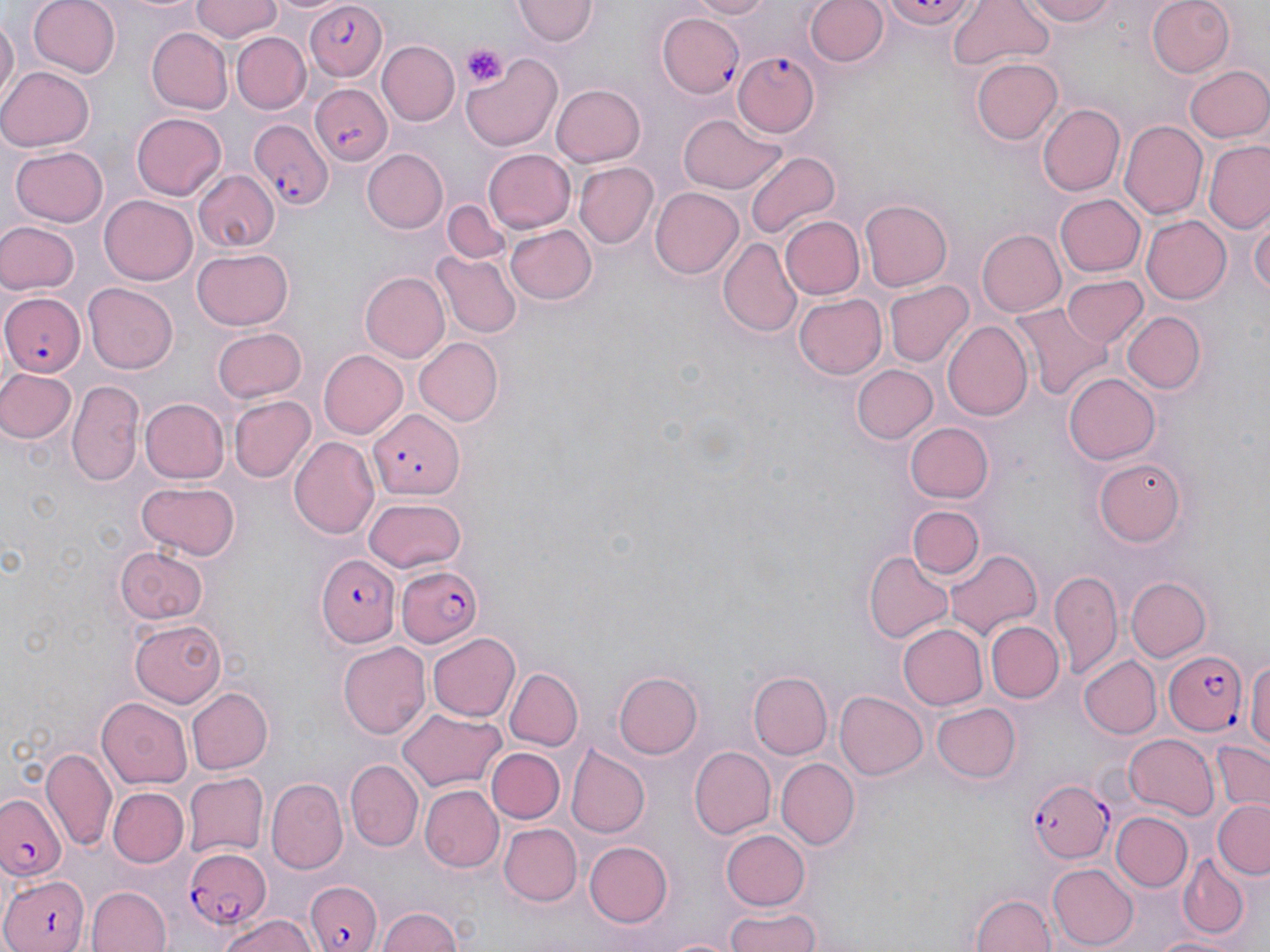

Summary:
  - Coordinate format: approximate bounding boxes as (x1, y1, x2, y2) in pixels
  - Plasmodium falciparum-infected red blood cell locations: (881, 0, 978, 30), (303, 3, 386, 82), (732, 50, 819, 137), (310, 85, 392, 166), (247, 117, 332, 213), (0, 289, 84, 378), (371, 409, 464, 495), (315, 555, 400, 646), (395, 565, 483, 645), (1164, 649, 1251, 736), (1028, 778, 1113, 864), (0, 794, 65, 884), (180, 842, 271, 936), (0, 874, 90, 952), (304, 878, 383, 952)
  - Platelet locations: (461, 43, 508, 91)
  - Uninfected red blood cell locations: (26, 0, 119, 78), (190, 0, 282, 44), (691, 0, 775, 20), (805, 0, 890, 70), (1018, 0, 1124, 26), (1147, 0, 1234, 76), (515, 1, 600, 45), (948, 1, 1054, 71), (0, 12, 17, 110), (660, 13, 745, 99), (145, 27, 231, 114), (233, 32, 310, 113), (378, 41, 459, 126), (462, 51, 563, 150), (972, 57, 1063, 144), (1184, 65, 1270, 143), (0, 66, 95, 151), (550, 83, 646, 167), (1040, 103, 1126, 196), (131, 112, 228, 200), (676, 114, 785, 195), (1121, 120, 1208, 220), (1205, 141, 1270, 234), (10, 144, 108, 228), (484, 148, 576, 233), (363, 149, 447, 234), (745, 149, 841, 242), (572, 163, 657, 248), (193, 169, 279, 252), (648, 187, 744, 280), (101, 193, 197, 282), (1055, 193, 1146, 277), (859, 199, 951, 292), (444, 202, 514, 265), (1249, 215, 1270, 303), (778, 216, 864, 300), (1142, 217, 1230, 303), (0, 222, 76, 295), (504, 224, 596, 306), (976, 229, 1067, 317), (717, 237, 801, 336), (192, 247, 295, 330), (434, 252, 522, 339), (360, 272, 448, 363), (1061, 275, 1148, 349), (885, 280, 973, 366), (84, 283, 178, 374), (794, 294, 887, 379), (1010, 305, 1109, 398), (1123, 311, 1206, 395), (943, 321, 1033, 421), (213, 326, 306, 403), (415, 337, 504, 426), (318, 351, 407, 439), (851, 364, 939, 444), (0, 369, 76, 446), (1063, 372, 1160, 465), (68, 379, 145, 490), (230, 395, 314, 483), (139, 398, 230, 483), (907, 423, 993, 503), (291, 437, 380, 538), (1092, 455, 1189, 546), (135, 482, 240, 560), (362, 497, 467, 574), (906, 505, 984, 579), (907, 512, 1031, 604), (115, 545, 209, 624), (945, 548, 1039, 640), (865, 552, 954, 644), (1050, 568, 1123, 676), (1124, 577, 1211, 663), (128, 619, 229, 706), (984, 621, 1063, 703), (898, 622, 987, 711), (428, 633, 521, 721), (338, 641, 430, 739), (1246, 653, 1270, 762), (1077, 655, 1160, 739), (504, 668, 584, 751), (613, 671, 703, 759), (748, 672, 832, 759), (186, 686, 271, 774), (834, 690, 928, 780), (98, 698, 192, 788), (932, 701, 1020, 783), (399, 708, 504, 791), (1122, 732, 1217, 817), (1208, 738, 1270, 814), (690, 747, 776, 837), (42, 748, 115, 850), (488, 748, 564, 823), (566, 748, 648, 838), (774, 757, 860, 850), (347, 759, 422, 850), (182, 772, 266, 859), (267, 779, 348, 873), (422, 786, 503, 872), (109, 788, 188, 868), (1212, 799, 1270, 878), (1109, 812, 1192, 892), (500, 824, 582, 905), (721, 829, 811, 911), (583, 840, 673, 928), (1177, 856, 1249, 938), (1047, 865, 1137, 947), (89, 885, 170, 952), (970, 891, 1056, 952), (376, 906, 465, 952), (718, 908, 826, 951), (215, 911, 319, 952), (1149, 931, 1248, 952)
  - Slide-level diagnosis: Plasmodium falciparum
  - Stain: May-Grünwald-Giemsa
  - Image size: 1270×952 pixels
  - Magnification: 1000x
  - Preparation: thin blood smear
  - Modality: optical microscopy
  - Field of view: single